Which red blood cells are Plasmodium falciparum-infected, and which are of indeterminate infection status?
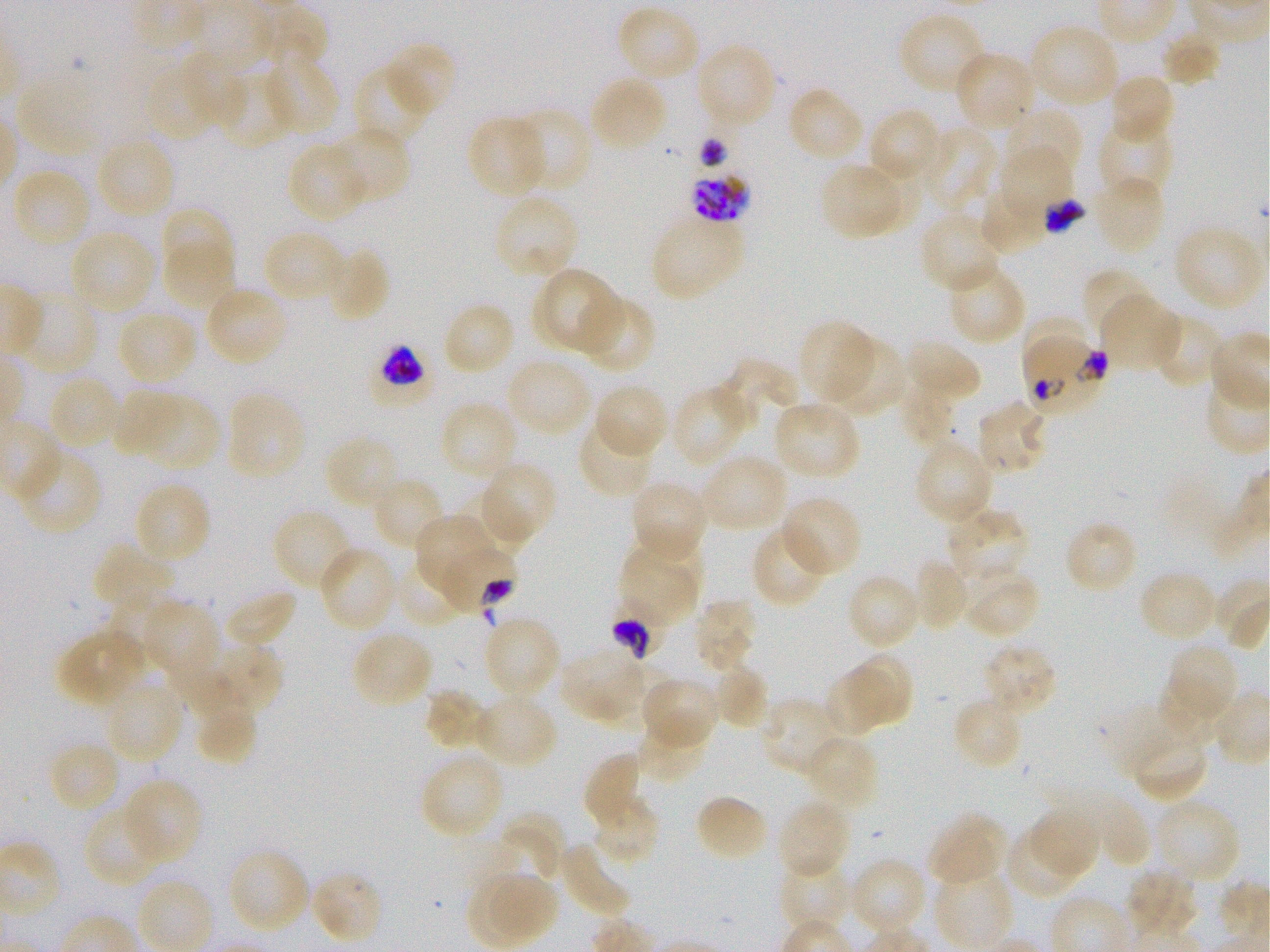

Approximate bounding boxes as {x1, y1, x2, y2} in pixels. Not every red blood cell is marked. A life-cycle stage — or a range of stages, where the recorded stages span more than one — follows each staged infected red blood cell.
Infected red blood cells: {691, 168, 750, 223} schizont; {1042, 196, 1085, 234} late trophozoite to early schizont; {1025, 337, 1102, 416}; {375, 345, 428, 397} trophozoite.
Red blood cells of indeterminate infection status: {439, 541, 517, 617}, {611, 604, 666, 660}.

locations of uninfected red blood cells = {615, 4, 701, 83}, {256, 7, 327, 70}, {898, 11, 990, 96}, {1029, 23, 1119, 108}, {1160, 30, 1224, 88}, {387, 42, 457, 118}, {695, 42, 778, 129}, {182, 50, 244, 128}, {953, 50, 1036, 131}, {264, 52, 340, 136}, {144, 61, 216, 143}, {353, 64, 431, 146}, {216, 70, 292, 151}, {16, 73, 100, 157}, {1107, 73, 1174, 145}, {588, 75, 668, 153}, {787, 86, 865, 165}, {1003, 106, 1083, 181}, {508, 109, 592, 194}, {872, 113, 937, 181}, {466, 115, 548, 197}, {1098, 117, 1173, 198}, {328, 126, 412, 204}, {922, 126, 998, 214}, {95, 134, 177, 220}, {286, 142, 369, 222}, {999, 148, 1072, 218}, {11, 167, 91, 250}, {821, 167, 899, 240}, {1094, 174, 1166, 254}, {977, 184, 1046, 255}, {492, 193, 580, 281}, {161, 206, 234, 280}, {919, 211, 1002, 295}, {650, 215, 744, 301}, {1173, 223, 1263, 312}, {68, 228, 155, 314}, {262, 229, 345, 304}, {163, 240, 234, 309}, {324, 245, 391, 323}, {946, 263, 1028, 346}, {543, 267, 622, 352}, {1082, 267, 1153, 343}, {203, 286, 289, 366}, {18, 288, 98, 375}, {1102, 294, 1181, 371}, {577, 295, 657, 374}, {441, 301, 515, 377}, {117, 308, 198, 385}, {1149, 313, 1225, 389}, {1021, 318, 1086, 382}, {798, 319, 875, 404}, {824, 336, 908, 416}, {904, 339, 982, 406}, {505, 356, 593, 438}, {718, 358, 798, 424}, {47, 375, 121, 450}, {593, 383, 670, 459}, {671, 383, 752, 468}, {899, 385, 955, 446}, {111, 388, 181, 458}, {226, 392, 307, 480}, {142, 395, 219, 470}, {439, 400, 518, 482}, {772, 400, 862, 480}, {977, 400, 1050, 476}, {576, 420, 657, 498}, {323, 434, 402, 511}, {913, 439, 995, 526}, {16, 446, 103, 536}, {700, 453, 787, 533}, {480, 461, 558, 546}, {371, 476, 448, 551}, {628, 478, 709, 561}, {134, 479, 213, 564}, {781, 495, 863, 578}, {946, 505, 1032, 582}, {270, 506, 356, 592}, {414, 514, 494, 595}, {1063, 520, 1139, 595}, {750, 524, 828, 609}, {619, 541, 701, 623}, {92, 542, 175, 612}, {318, 546, 398, 633}, {393, 556, 469, 627}, {912, 559, 970, 632}, {962, 566, 1039, 637}, {1137, 570, 1219, 643}, {846, 572, 921, 651}, {224, 587, 298, 649}, {107, 592, 174, 663}, {692, 598, 757, 673}, {142, 599, 219, 680}, {482, 616, 562, 699}, {57, 629, 147, 708}, {351, 630, 434, 709}, {210, 643, 284, 716}, {981, 643, 1060, 716}, {1164, 643, 1240, 720}, {560, 647, 641, 722}, {168, 649, 243, 717}, {850, 651, 912, 724}, {711, 664, 769, 730}, {593, 667, 678, 727}, {823, 670, 883, 738}, {640, 677, 720, 750}, {103, 678, 184, 765}, {1158, 680, 1220, 741}, {424, 688, 488, 751}, {474, 694, 558, 770}, {194, 695, 257, 766}, {758, 696, 842, 776}, {952, 696, 1023, 771}, {1100, 704, 1195, 778}, {635, 716, 709, 783}, {1130, 732, 1209, 804}, {804, 734, 879, 811}, {47, 739, 121, 814}, {581, 751, 642, 827}, {418, 752, 505, 839}, {122, 778, 202, 864}, {589, 793, 661, 867}, {1082, 793, 1150, 869}, {693, 794, 769, 862}, {1154, 798, 1242, 885}, {777, 799, 850, 881}, {84, 805, 164, 888}, {1029, 809, 1099, 878}, {500, 812, 565, 885}, {928, 812, 1006, 889}, {1004, 827, 1080, 901}, {560, 841, 633, 919}, {226, 847, 311, 935}, {850, 857, 929, 936}, {778, 860, 852, 932}, {932, 864, 1012, 947}, {1124, 866, 1199, 941}, {310, 868, 385, 945}, {495, 873, 558, 939}
life-cycle stages observed = trophozoite, schizont
stain = Giemsa
preparation = thin blood film
culture = static in-vitro Plasmodium falciparum strain 3D7
field of view = one from this slide
image size = 1270×952 pixels
donor blood group = O+
objective = 100x, oil immersion, numerical aperture 1.25